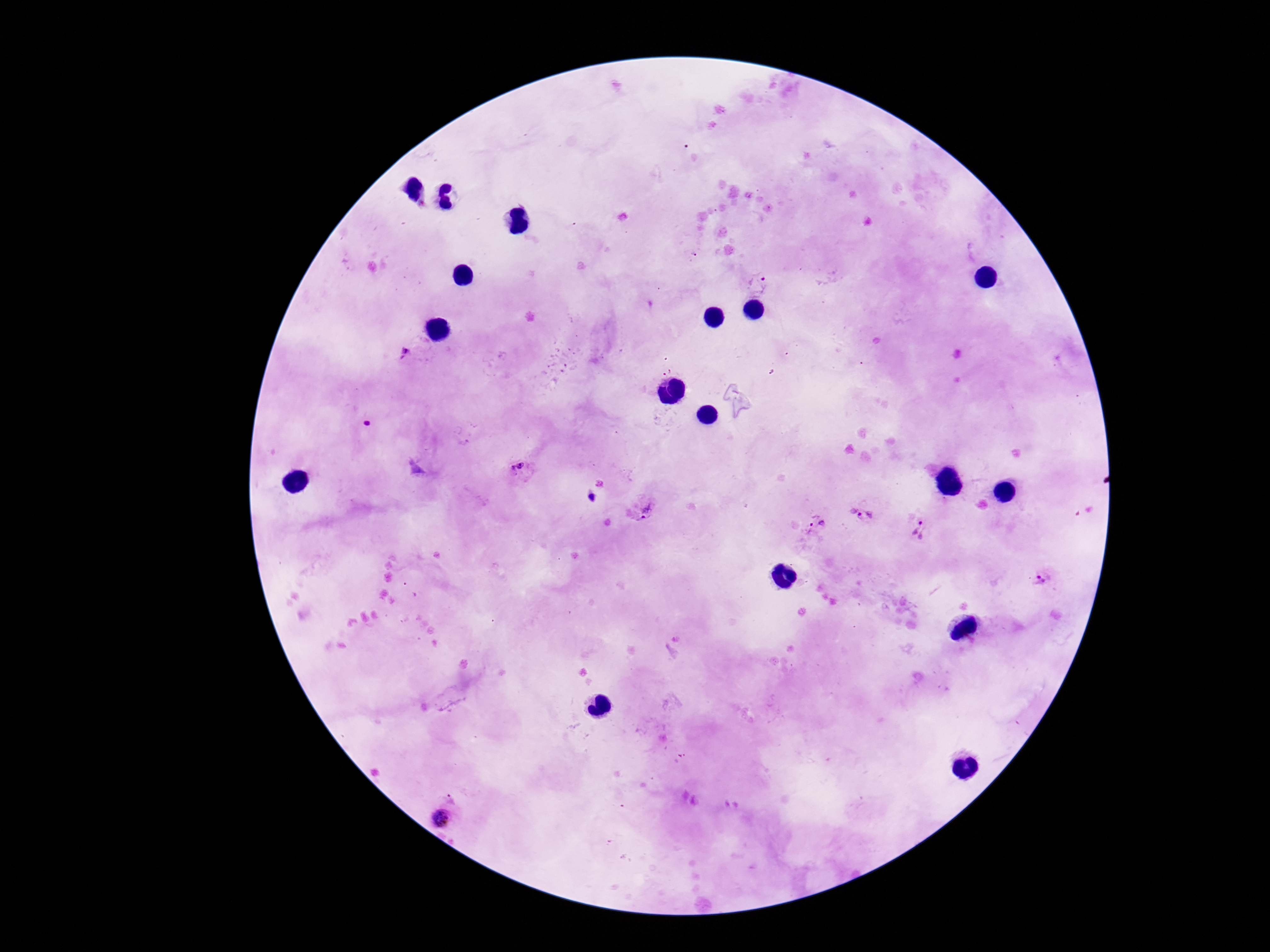

image size = 1270×952 pixels
field of view = single
stain = Giemsa
magnification = 100x
patient malaria status = positive
preparation = thick blood smear
Plasmodium parasite locations = approximate centers as [x, y] in pixels: [759, 284], [404, 355], [367, 423], [520, 471], [640, 508], [869, 518], [813, 527], [918, 530], [1043, 581], [444, 817]
capture = smartphone camera through the microscope eyepiece